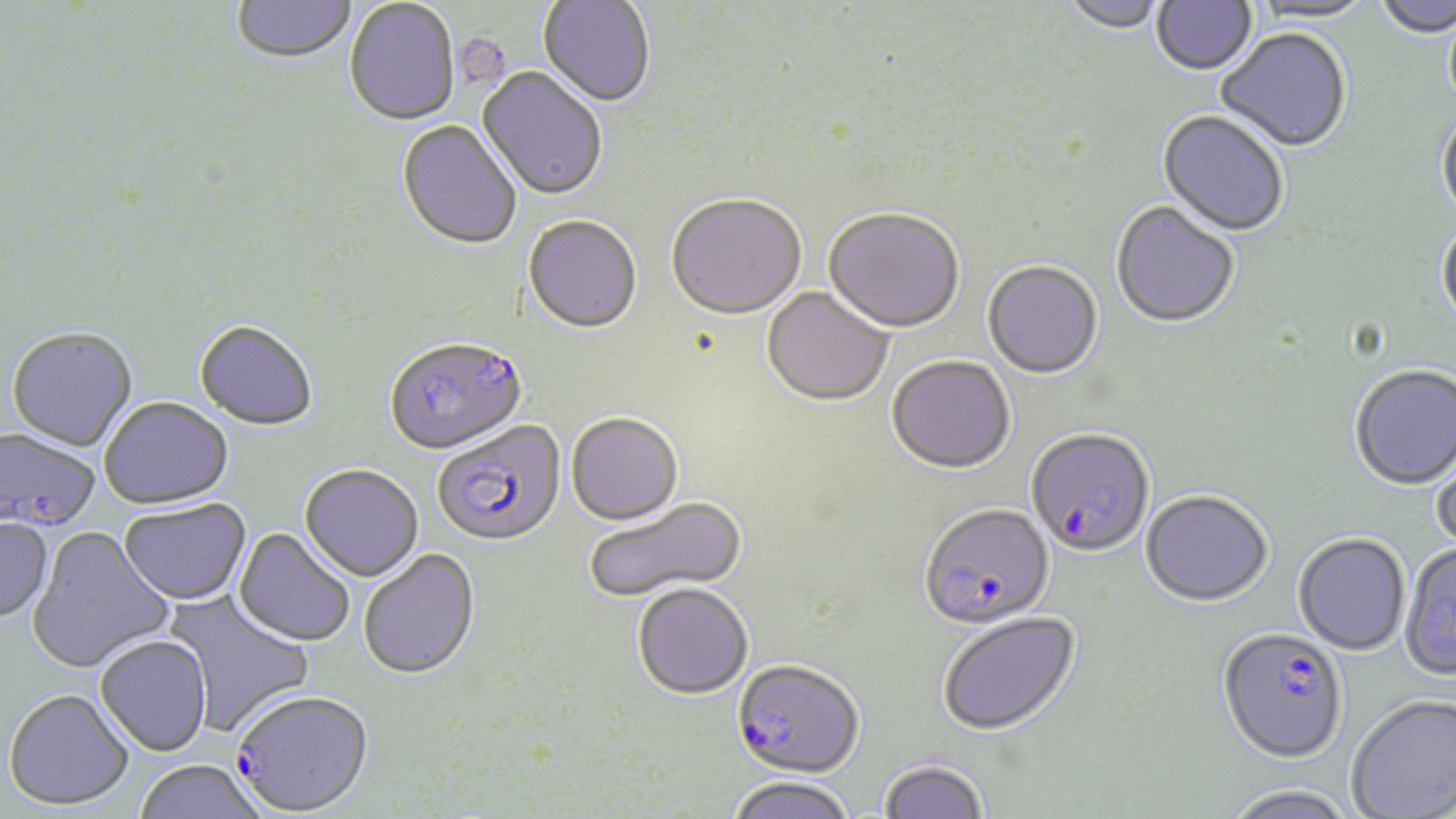
Summary:
  - Coordinate format: approximate bounding boxes as named x1/y1/x2/y2 corners in pixels
  - Platelet locations: (x1=461, y1=38, x2=517, y2=97)
  - Uninfected red blood cell locations: (x1=1060, y1=0, x2=1168, y2=36), (x1=1152, y1=0, x2=1257, y2=79), (x1=1372, y1=0, x2=1456, y2=39), (x1=232, y1=1, x2=357, y2=66), (x1=344, y1=1, x2=460, y2=128), (x1=538, y1=1, x2=655, y2=110), (x1=1246, y1=1, x2=1377, y2=26), (x1=1443, y1=9, x2=1456, y2=121), (x1=1216, y1=29, x2=1352, y2=154), (x1=476, y1=67, x2=608, y2=203), (x1=1157, y1=111, x2=1288, y2=239), (x1=1437, y1=111, x2=1456, y2=223), (x1=397, y1=121, x2=522, y2=252), (x1=666, y1=196, x2=806, y2=323), (x1=1110, y1=202, x2=1240, y2=331), (x1=823, y1=210, x2=964, y2=336), (x1=523, y1=217, x2=643, y2=337), (x1=1437, y1=219, x2=1456, y2=335), (x1=982, y1=262, x2=1103, y2=381), (x1=761, y1=288, x2=893, y2=409), (x1=193, y1=322, x2=318, y2=433), (x1=6, y1=329, x2=137, y2=453), (x1=886, y1=358, x2=1016, y2=478), (x1=1349, y1=366, x2=1456, y2=492), (x1=99, y1=398, x2=234, y2=512), (x1=566, y1=415, x2=683, y2=527), (x1=1430, y1=435, x2=1456, y2=558), (x1=299, y1=466, x2=424, y2=583), (x1=1140, y1=492, x2=1273, y2=609), (x1=586, y1=496, x2=749, y2=605), (x1=119, y1=499, x2=252, y2=606), (x1=0, y1=517, x2=54, y2=623), (x1=26, y1=526, x2=175, y2=675), (x1=234, y1=527, x2=356, y2=648), (x1=1292, y1=534, x2=1411, y2=657), (x1=1400, y1=543, x2=1454, y2=683), (x1=359, y1=549, x2=481, y2=682), (x1=631, y1=585, x2=754, y2=701), (x1=161, y1=590, x2=314, y2=737), (x1=937, y1=613, x2=1083, y2=739), (x1=95, y1=635, x2=212, y2=756), (x1=3, y1=688, x2=134, y2=811), (x1=1346, y1=694, x2=1456, y2=818), (x1=877, y1=759, x2=990, y2=819), (x1=134, y1=761, x2=268, y2=819), (x1=726, y1=778, x2=859, y2=819), (x1=1221, y1=785, x2=1358, y2=819)
  - Plasmodium falciparum-infected red blood cell locations: (x1=384, y1=339, x2=527, y2=458), (x1=433, y1=421, x2=567, y2=550), (x1=0, y1=428, x2=100, y2=534), (x1=1026, y1=430, x2=1155, y2=560), (x1=918, y1=506, x2=1055, y2=632), (x1=1217, y1=629, x2=1347, y2=765), (x1=731, y1=663, x2=863, y2=781), (x1=233, y1=691, x2=375, y2=817)
  - Slide-level diagnosis: Plasmodium falciparum
  - Magnification: 1000x
  - Modality: light microscopy
  - Stain: May-Grünwald-Giemsa
  - Preparation: thin blood film
  - Image size: 1456×819 pixels
  - Field of view: one of a larger specimen